Report the malaria status of this cell.
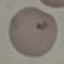
Uninfected.

{
  "image_type": "automatically extracted cell patch, resized to 64 × 64 pixels",
  "preparation": "thin blood film",
  "stain": "Giemsa",
  "capture": "smartphone through the microscope eyepiece"
}